Assess this cell for malaria.
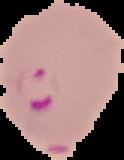
Parasitized.

Summary:
  - Preparation: thin blood film
  - Image type: cell region segmented out of the field of view; surrounding area masked to black
  - Image size: 124×160 pixels